Locate and identify every blood parasite.
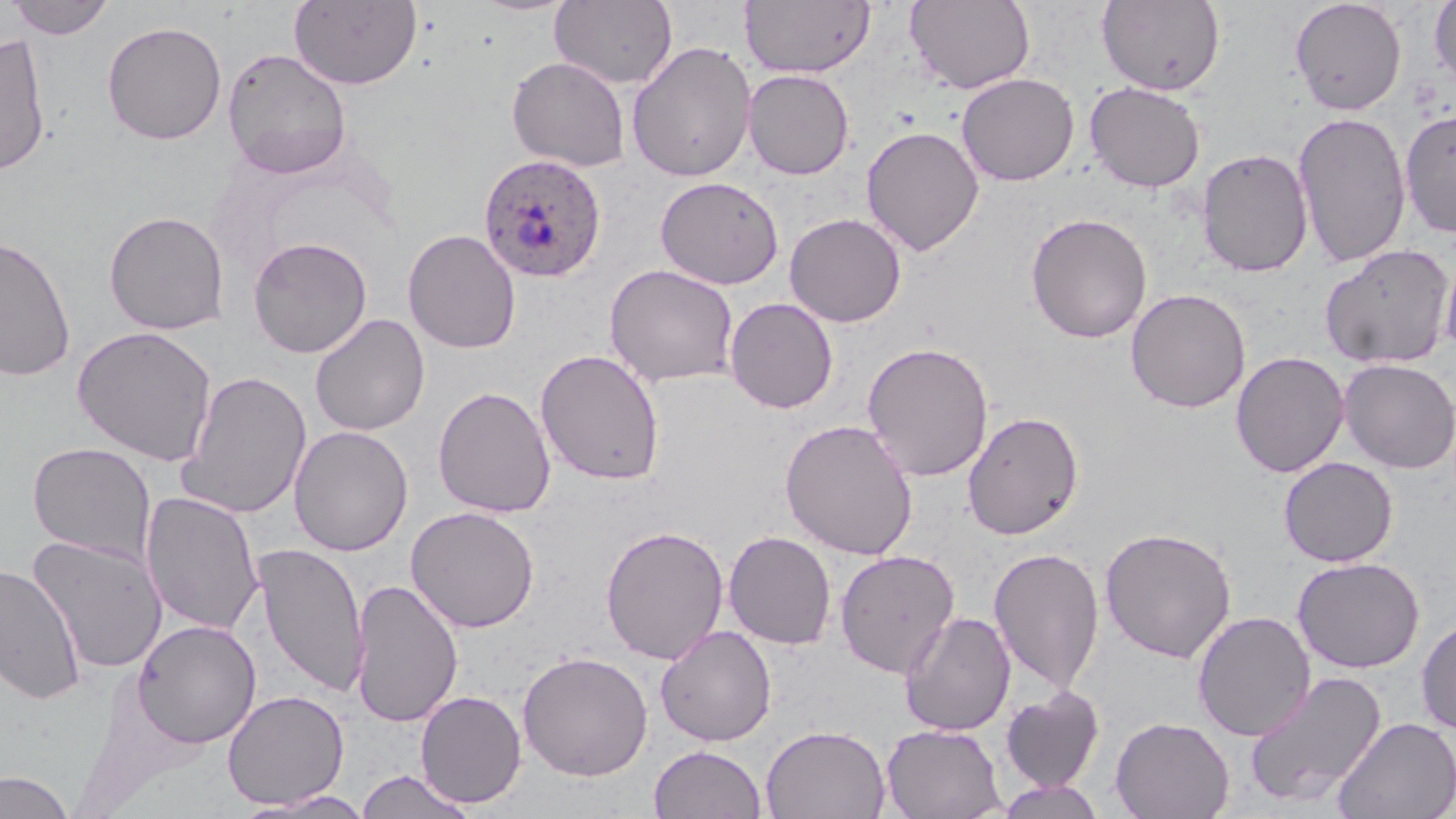

Approximate bounding boxes as (x1, y1, x2, y2) in pixels.
Plasmodium ovale-infected red blood cells: (478, 152, 607, 282).
No Plasmodium falciparum, Plasmodium malariae, Plasmodium vivax, Babesia divergens, or Trypanosoma brucei observed.

Summary:
  - Uninfected red blood cell locations: (7, 0, 115, 40), (289, 0, 423, 90), (550, 0, 678, 90), (741, 0, 876, 78), (906, 0, 1035, 93), (1096, 0, 1225, 96), (1290, 0, 1407, 115), (1428, 1, 1456, 94), (102, 20, 227, 145), (0, 31, 52, 176), (627, 41, 757, 183), (222, 48, 352, 177), (506, 56, 631, 172), (742, 69, 854, 179), (957, 73, 1079, 186), (1084, 81, 1206, 193), (1400, 109, 1456, 237), (1292, 112, 1412, 268), (861, 125, 984, 256), (1197, 147, 1313, 277), (655, 176, 784, 290), (103, 210, 229, 335), (784, 212, 907, 327), (1025, 213, 1152, 343), (403, 229, 521, 354), (0, 235, 76, 382), (247, 236, 372, 359), (1320, 243, 1456, 369), (1439, 245, 1456, 360), (604, 264, 739, 388), (1125, 288, 1251, 413), (724, 297, 838, 414), (309, 313, 430, 436), (73, 325, 217, 466), (862, 341, 994, 482), (535, 348, 665, 486), (1230, 351, 1349, 478), (1338, 358, 1456, 474), (178, 370, 311, 520), (433, 385, 556, 519), (963, 410, 1084, 540), (779, 419, 919, 560), (289, 425, 413, 557), (28, 441, 156, 564), (1278, 456, 1398, 567), (140, 490, 264, 637), (406, 506, 540, 633), (600, 525, 729, 665), (1099, 526, 1237, 663), (723, 531, 836, 650), (26, 535, 169, 674), (253, 542, 368, 698), (988, 547, 1105, 695), (834, 549, 961, 679), (1292, 557, 1426, 673), (0, 563, 85, 703), (350, 577, 463, 728), (899, 611, 1016, 736), (1192, 611, 1316, 741), (1416, 617, 1456, 735), (133, 619, 262, 747), (656, 625, 777, 746), (517, 650, 654, 781), (1243, 670, 1388, 809), (1000, 687, 1105, 793), (222, 689, 350, 809), (415, 690, 527, 808), (1110, 716, 1234, 819), (1333, 716, 1456, 819), (761, 724, 890, 819), (881, 724, 1006, 819), (649, 744, 767, 818), (355, 770, 477, 818), (0, 771, 75, 819), (996, 779, 1107, 819), (238, 790, 377, 818)
  - Slide-level diagnosis: Plasmodium ovale
  - Image size: 1456×819 pixels
  - Stain: May-Grünwald-Giemsa
  - Field of view: single
  - Preparation: thin blood film
  - Magnification: 1000x
  - Modality: optical microscopy